Classify this cell by malaria status.
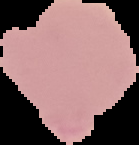
It is uninfected.

Image is 139×145 pixels. From a thin blood film. Segmented cell region on a black background.